Assess this cell for malaria.
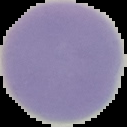

Uninfected.

Summary:
  - Image size: 127×127 pixels
  - Preparation: thin blood film
  - Image type: segmented cell region with the area outside set to black